Mark where platelets are.
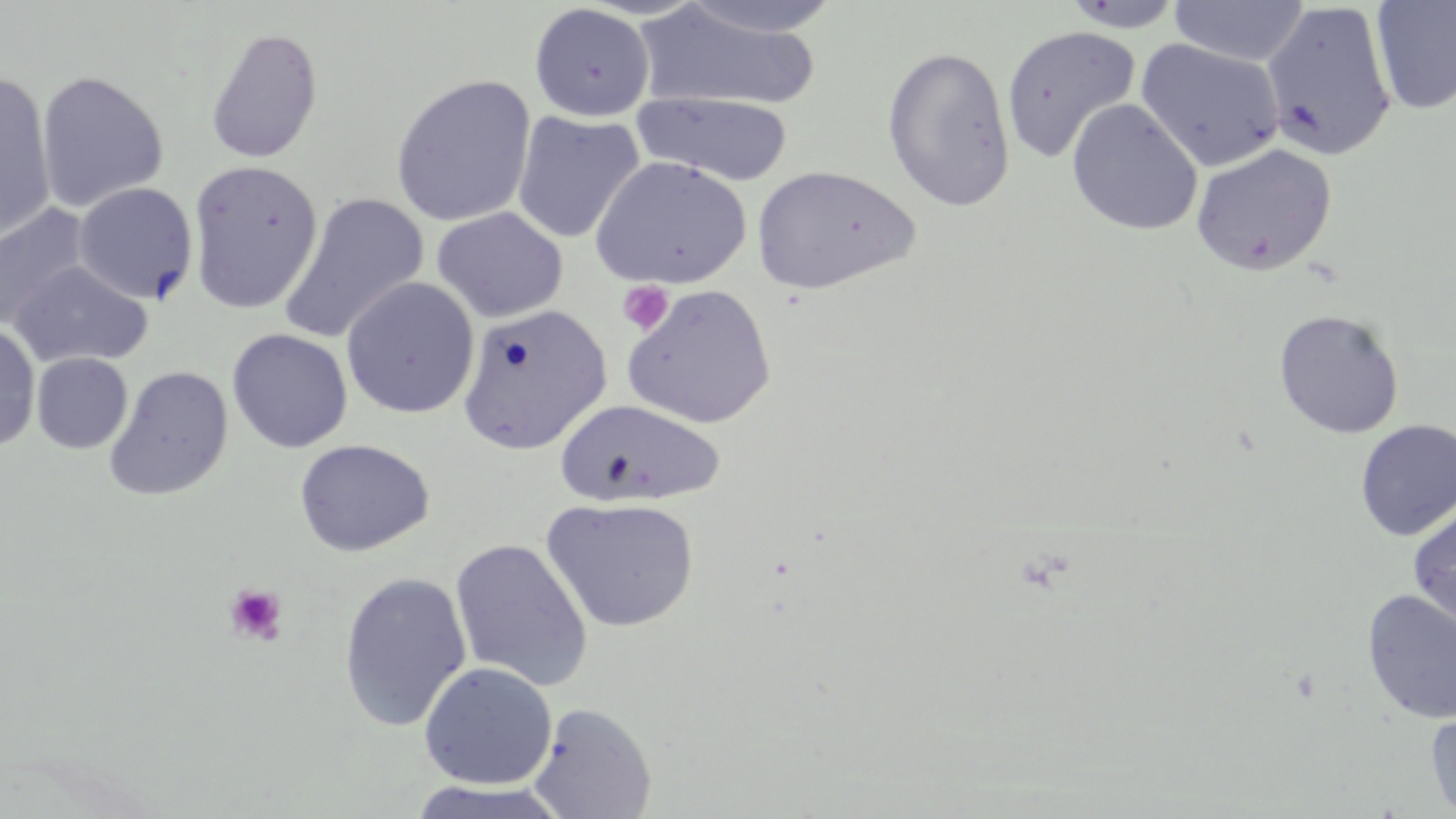

Approximate bounding boxes as [x1, y1, x2, y2] in pixels.
Platelets: [617, 281, 674, 335], [223, 583, 288, 645].

slide-level diagnosis = no evidence of blood parasites
image size = 1456×819 pixels
field of view = one of a larger specimen
preparation = thin blood smear
modality = light microscopy
uninfected red blood cell locations = approximate bounding boxes as [x1, y1, x2, y2] in pixels: [674, 0, 843, 39], [1060, 0, 1186, 32], [1169, 0, 1310, 67], [1371, 0, 1456, 115], [1261, 2, 1397, 161], [528, 3, 655, 122], [633, 3, 822, 114], [1001, 25, 1141, 164], [205, 27, 323, 164], [1135, 38, 1285, 173], [881, 44, 1015, 212], [0, 70, 56, 244], [36, 70, 169, 213], [389, 74, 536, 228], [630, 90, 794, 186], [1066, 99, 1203, 236], [511, 110, 645, 245], [1190, 143, 1337, 276], [591, 155, 751, 289], [187, 159, 324, 314], [751, 166, 918, 295], [73, 183, 198, 304], [278, 192, 429, 345], [0, 203, 92, 332], [431, 206, 568, 323], [9, 261, 153, 368], [341, 277, 479, 418], [621, 284, 776, 429], [456, 302, 611, 455], [1274, 309, 1404, 439], [0, 321, 41, 453], [227, 328, 352, 453], [31, 352, 132, 454], [104, 365, 233, 501], [555, 398, 725, 509], [1354, 419, 1456, 541], [294, 438, 434, 557], [541, 496, 699, 632], [1407, 504, 1456, 629], [450, 538, 593, 692], [337, 570, 472, 733], [1361, 590, 1456, 725], [419, 661, 557, 789], [527, 702, 657, 819], [1425, 708, 1456, 817], [399, 779, 576, 819]
stain = May-Grünwald-Giemsa
magnification = 1000x